Report the malaria status of this cell.
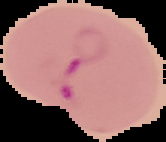

Parasitized.

Cell region segmented out of the field of view; the surrounding area is masked to black. From a thin blood smear. Image is 166×142 pixels.